State which parasite is depicted.
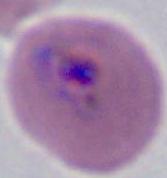

Plasmodium.

Summary:
  - Magnification: 400x or 1000x
  - Modality: micrograph